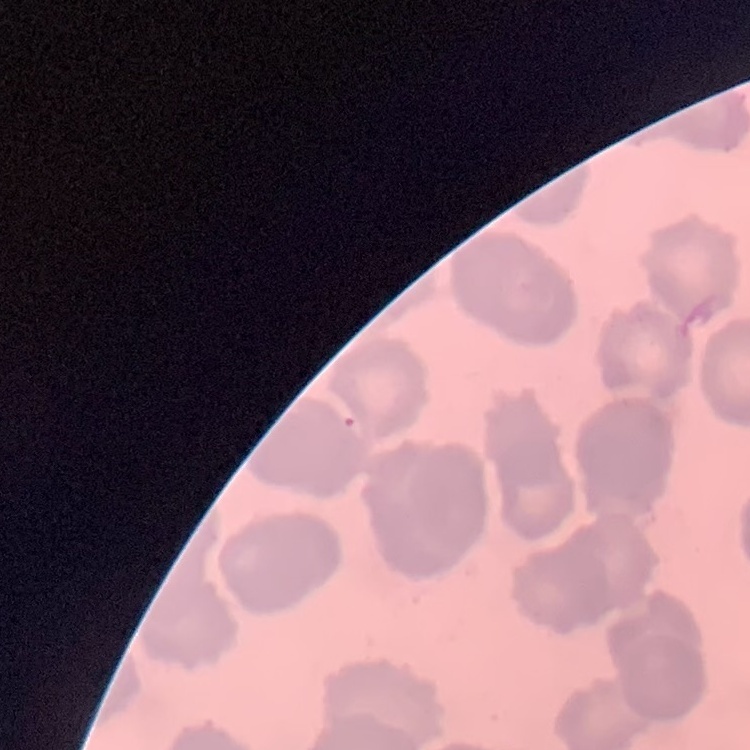

red_blood_cell_morphology: rouleaux formation
stain: Field's or Giemsa
preparation: thin blood smear
image_type: square crop of a larger photomicrograph